Describe the morphology of the erythrocytes.
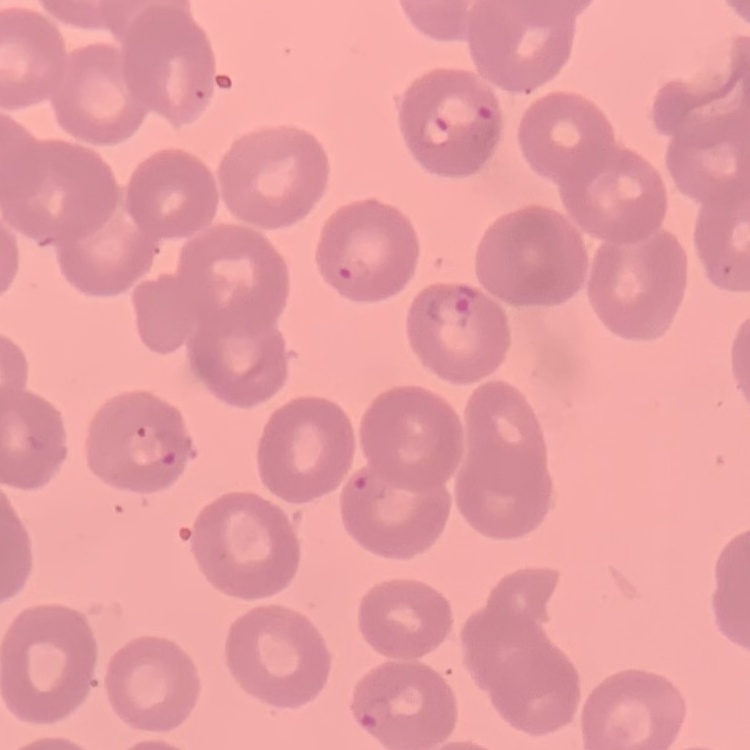

No rouleaux formation.

Stained with either Field's or Giemsa. Square crop of a larger photomicrograph. Thin blood smear.